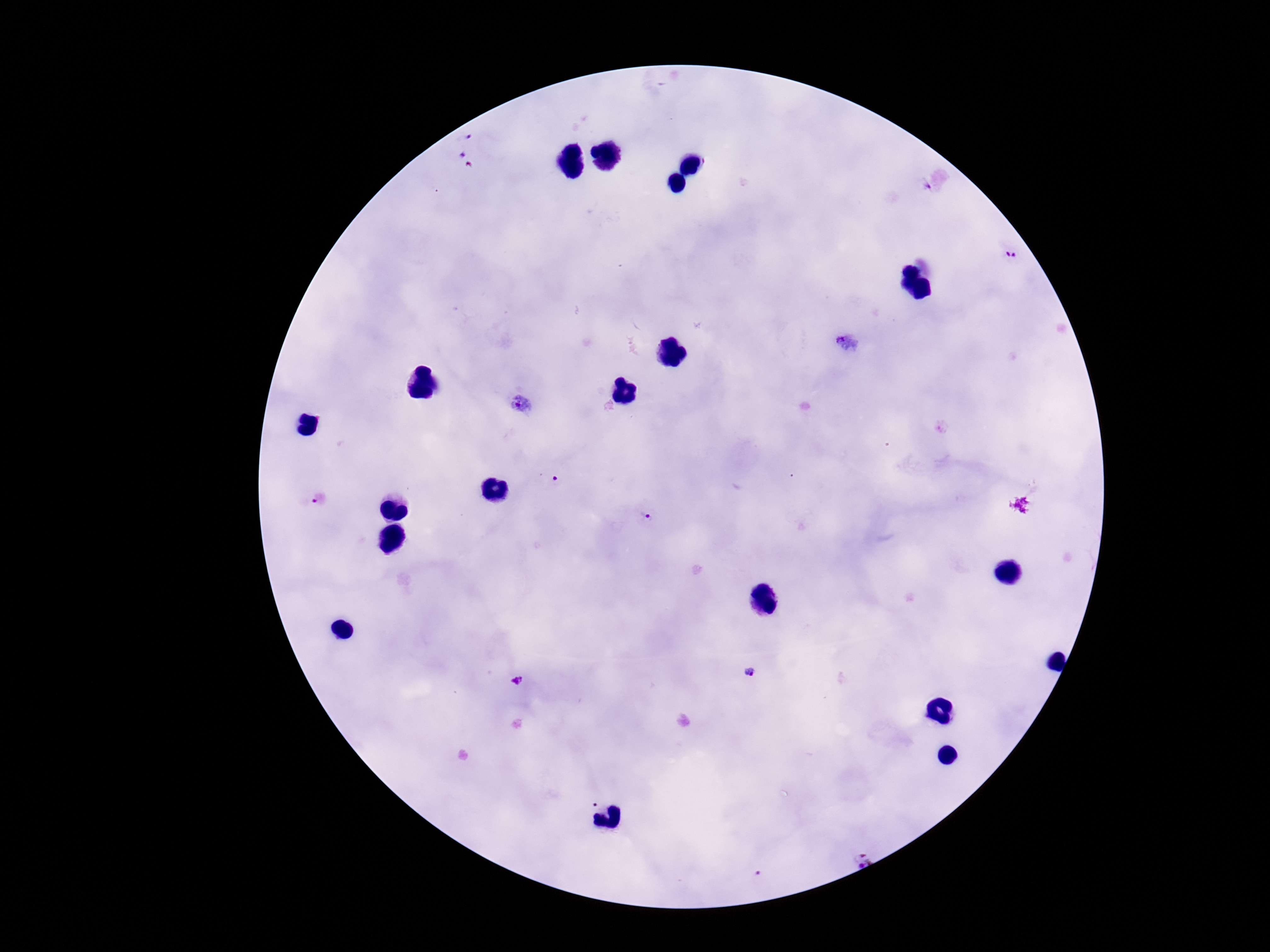

{
  "magnification": "100x",
  "field_of_view": "single",
  "capture": "smartphone camera through the microscope eyepiece",
  "preparation": "thick peripheral-blood smear",
  "stain": "Giemsa",
  "plasmodium_parasite_locations": "approximate object centers, in pixels from the top-left corner: (x=467, y=134), (x=458, y=152), (x=924, y=187), (x=1011, y=255), (x=849, y=342), (x=522, y=406), (x=553, y=479), (x=320, y=499), (x=648, y=519), (x=749, y=673), (x=518, y=681), (x=857, y=855), (x=759, y=875)",
  "image_size": "1270×952 pixels",
  "patient_malaria_status": "positive"
}